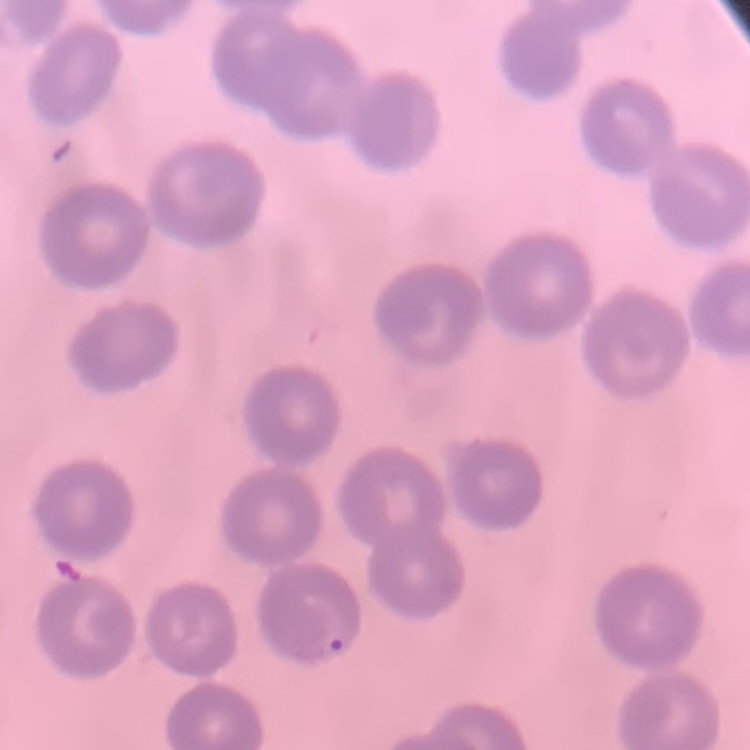

Summary:
  - Red blood cell morphology: no rouleaux formation
  - Stain: Field's or Giemsa
  - Preparation: thin blood smear
  - Image type: square crop of a larger photomicrograph